Identify the blood parasite species.
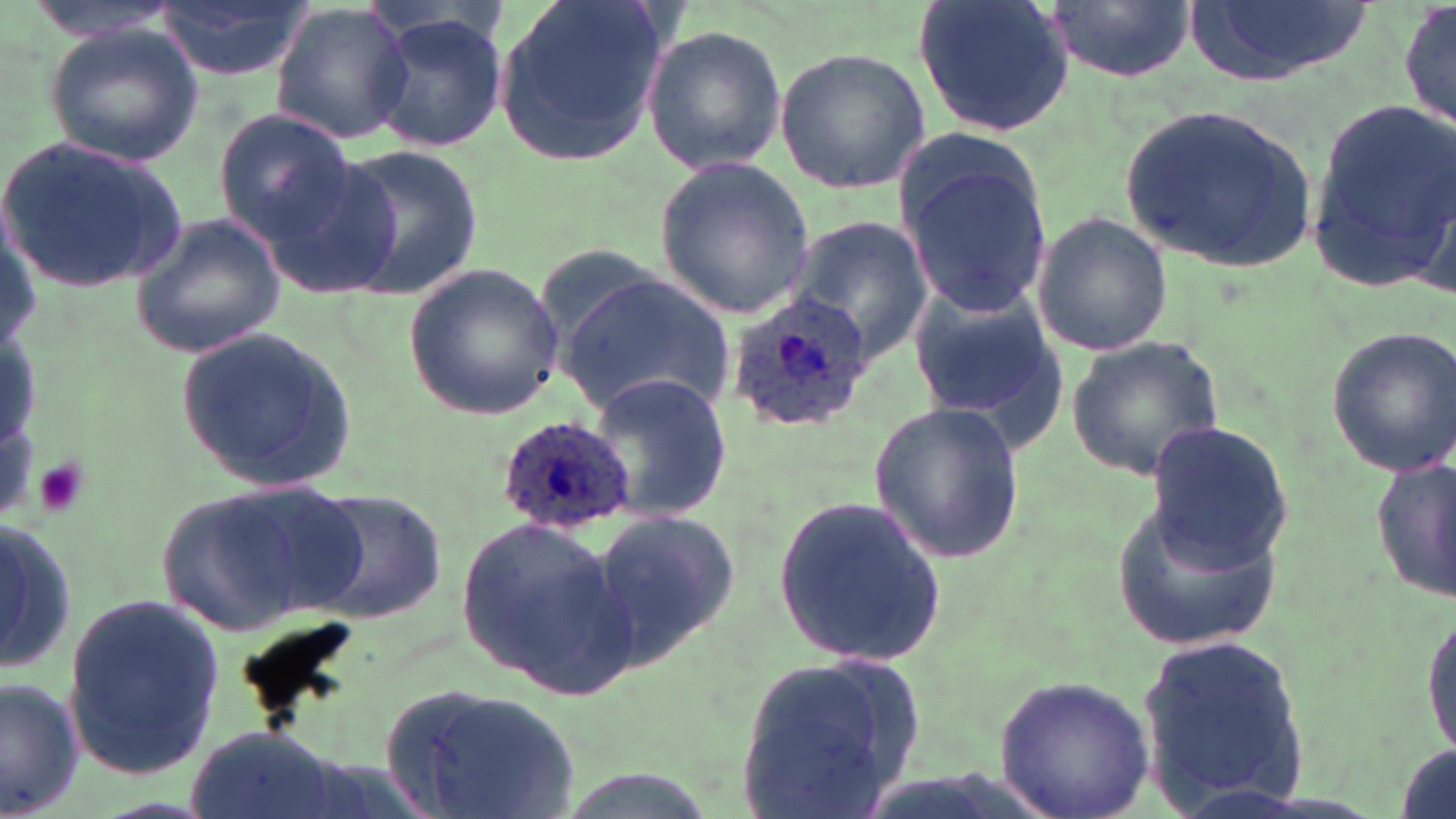
Plasmodium ovale.

Approximate bounding boxes as (x1, y1, x2, y2) in pixels. Plasmodium ovale-infected red blood cell locations: (724, 293, 875, 436), (497, 414, 637, 534). Platelet locations: (30, 455, 89, 520). Uninfected red blood cell locations: (149, 0, 316, 82), (490, 0, 672, 169), (914, 0, 1076, 138), (1045, 0, 1195, 85), (1181, 0, 1371, 89), (1396, 0, 1454, 139), (269, 4, 416, 146), (364, 10, 513, 154), (41, 22, 206, 167), (641, 24, 787, 177), (772, 46, 930, 194), (1118, 99, 1321, 275), (1301, 103, 1456, 291), (212, 110, 359, 247), (2, 137, 190, 293), (328, 144, 484, 299), (257, 148, 412, 301), (897, 154, 1056, 315), (653, 157, 818, 318), (1030, 211, 1173, 359), (131, 213, 289, 359), (790, 213, 934, 363), (404, 262, 565, 420), (562, 273, 735, 420), (904, 282, 1064, 446), (1323, 326, 1456, 478), (175, 327, 356, 492), (1065, 336, 1227, 481), (584, 372, 735, 522), (866, 401, 1027, 565), (1143, 420, 1293, 571), (1369, 455, 1455, 602), (151, 476, 369, 637), (305, 490, 448, 625), (775, 495, 947, 668), (1110, 501, 1283, 650), (586, 509, 743, 664), (454, 512, 637, 698), (0, 526, 76, 673), (61, 595, 227, 782), (1421, 600, 1456, 764), (1137, 636, 1313, 809), (733, 652, 925, 815), (990, 672, 1155, 819), (0, 678, 82, 818), (379, 683, 587, 819), (183, 722, 344, 819). One field of a larger specimen. May-Grünwald-Giemsa-stained preparation. Captured at 1000x magnification. Image is 1456×819 pixels. Optical microscopy. Thin blood film.